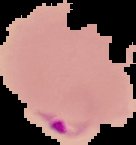

result = malaria parasites identified
preparation = thin blood film
image size = 136×145 pixels
image type = segmented cell region on a black background